Describe the morphology of the erythrocytes.
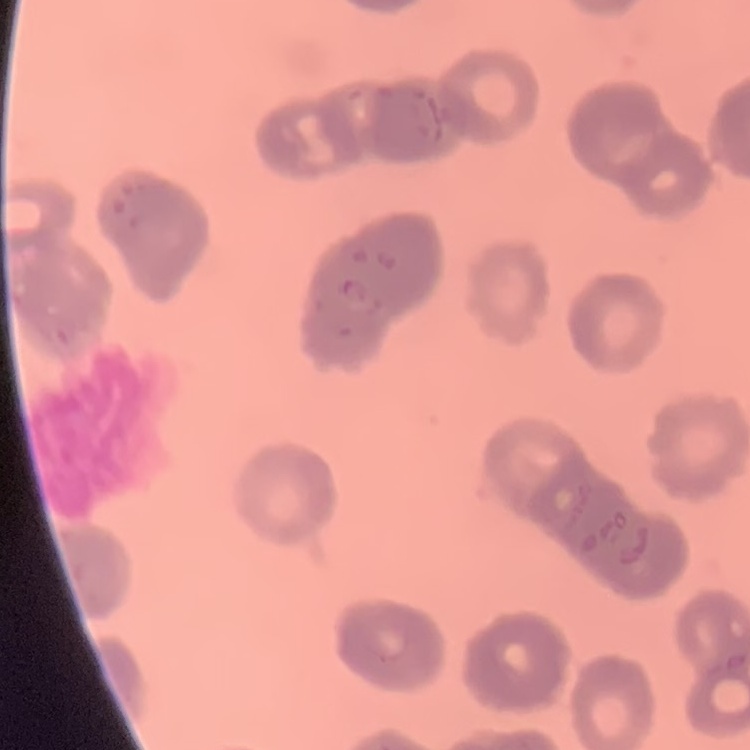
They show rouleaux formation.

Summary:
  - Image type: square crop of a larger photomicrograph
  - Preparation: thin peripheral smear
  - Stain: Field's or Giemsa